Report the malaria status of this cell.
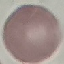
Uninfected.

image type = cell patch, automatically extracted from a larger field of view and resized to 64 × 64 pixels
capture = smartphone camera at the microscope eyepiece
preparation = thin blood smear
stain = Giemsa